Locate and identify every blood parasite.
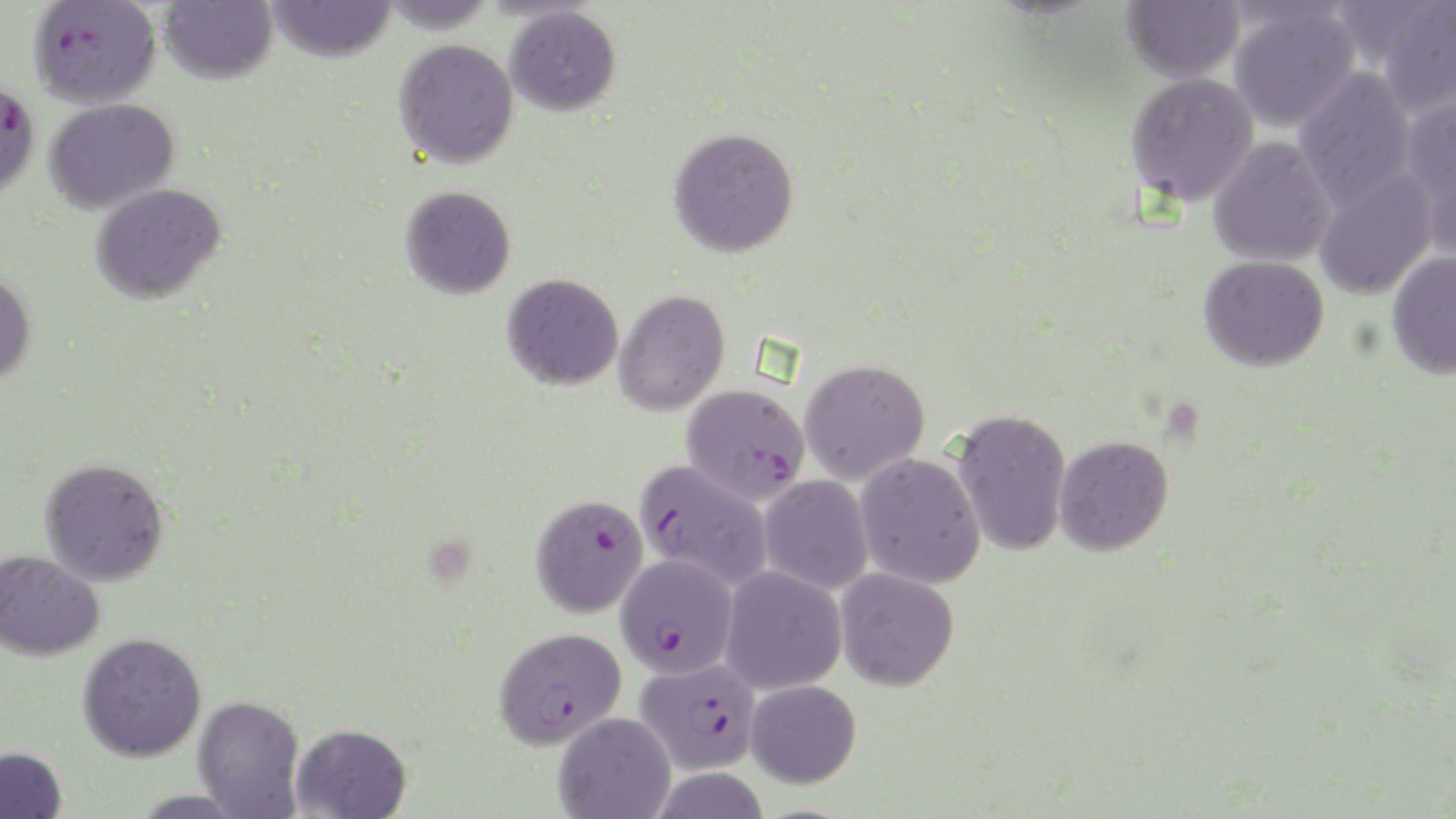
Approximate bounding boxes as named x1/y1/x2/y2 corners in pixels.
Plasmodium falciparum-infected red blood cells: (x1=28, y1=0, x2=161, y2=108), (x1=0, y1=77, x2=41, y2=205), (x1=682, y1=384, x2=810, y2=504), (x1=633, y1=459, x2=772, y2=591), (x1=530, y1=494, x2=647, y2=617), (x1=615, y1=553, x2=738, y2=678), (x1=493, y1=626, x2=627, y2=749), (x1=635, y1=657, x2=762, y2=775).
No Plasmodium ovale, Plasmodium malariae, Plasmodium vivax, Babesia divergens, or Trypanosoma brucei observed.

Uninfected red blood cell locations: (x1=159, y1=0, x2=277, y2=84), (x1=264, y1=0, x2=398, y2=62), (x1=1121, y1=0, x2=1245, y2=83), (x1=1376, y1=0, x2=1456, y2=119), (x1=504, y1=5, x2=621, y2=116), (x1=1229, y1=5, x2=1360, y2=132), (x1=392, y1=38, x2=519, y2=169), (x1=1293, y1=67, x2=1417, y2=210), (x1=1125, y1=72, x2=1259, y2=207), (x1=1401, y1=90, x2=1456, y2=247), (x1=44, y1=98, x2=180, y2=214), (x1=668, y1=126, x2=799, y2=257), (x1=1208, y1=137, x2=1336, y2=267), (x1=1312, y1=168, x2=1438, y2=300), (x1=90, y1=182, x2=226, y2=304), (x1=400, y1=185, x2=516, y2=299), (x1=1385, y1=250, x2=1456, y2=379), (x1=1198, y1=255, x2=1329, y2=372), (x1=0, y1=266, x2=36, y2=386), (x1=502, y1=273, x2=623, y2=390), (x1=613, y1=289, x2=729, y2=416), (x1=799, y1=358, x2=930, y2=485), (x1=950, y1=409, x2=1072, y2=557), (x1=1053, y1=435, x2=1173, y2=556), (x1=854, y1=453, x2=986, y2=589), (x1=40, y1=457, x2=170, y2=586), (x1=758, y1=475, x2=874, y2=595), (x1=0, y1=550, x2=105, y2=661), (x1=719, y1=566, x2=847, y2=695), (x1=834, y1=568, x2=959, y2=691), (x1=77, y1=632, x2=207, y2=762), (x1=745, y1=679, x2=861, y2=788), (x1=193, y1=695, x2=305, y2=818), (x1=552, y1=712, x2=676, y2=819), (x1=291, y1=723, x2=412, y2=818), (x1=0, y1=746, x2=68, y2=819). Platelet locations: (x1=1165, y1=402, x2=1207, y2=445), (x1=424, y1=541, x2=478, y2=585). Slide-level diagnosis: Plasmodium falciparum. Thin blood smear. Image is 1456×819 pixels. One field of a larger specimen. May-Grünwald-Giemsa-stained preparation. Light microscopy. Captured at 1000x magnification.